Assess this cell for malaria.
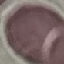

Uninfected.

Automatically extracted cell patch, resized to 64 × 64 pixels. Acquired by smartphone through the microscope eyepiece. Thin blood film. Giemsa-stained preparation.